Give the location of every parasitized red blood cell.
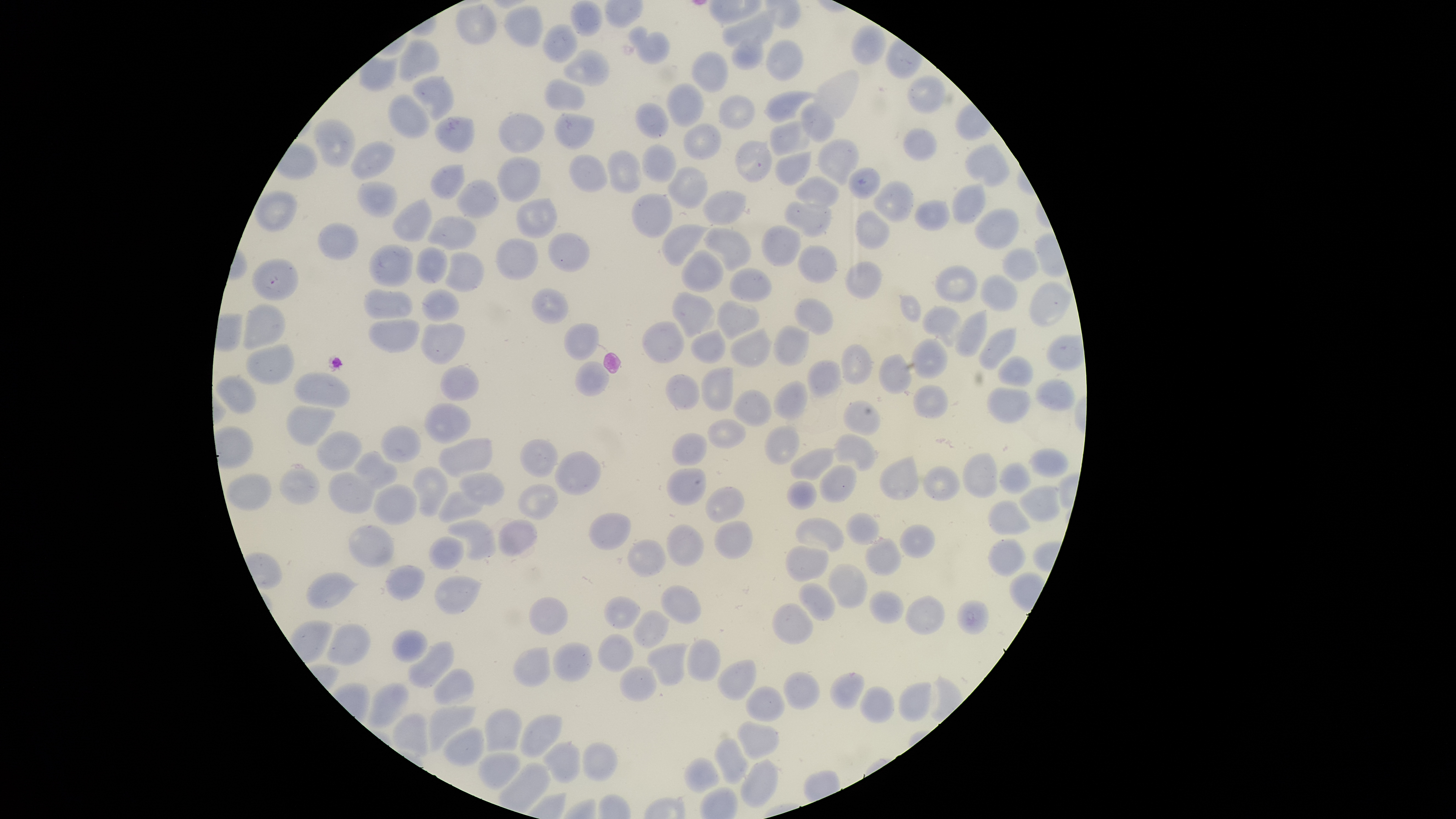
No parasitized red blood cells identified.

Approximate bounding boxes as [left, top, right, bottom] in pixels.
Summary:
  - Uninfected red blood cells: [569, 0, 604, 37], [455, 3, 497, 45], [722, 3, 779, 47], [504, 5, 543, 47], [542, 23, 577, 64], [851, 23, 886, 65], [628, 25, 670, 64], [731, 34, 765, 70], [398, 38, 440, 83], [765, 39, 804, 82], [563, 48, 611, 87], [691, 51, 729, 93], [907, 74, 947, 114], [411, 76, 455, 120], [543, 77, 587, 111], [666, 83, 704, 127], [764, 89, 818, 123], [388, 93, 431, 138], [718, 95, 755, 130], [635, 101, 669, 139], [800, 101, 836, 143], [498, 111, 545, 154], [554, 112, 594, 150], [434, 115, 475, 154], [313, 117, 356, 168], [769, 120, 814, 156], [683, 122, 722, 161], [903, 127, 937, 161], [816, 138, 861, 186], [349, 139, 396, 180], [734, 140, 773, 183], [964, 142, 1010, 187], [641, 144, 677, 182], [606, 150, 644, 194], [774, 151, 813, 187], [568, 154, 609, 193], [496, 155, 541, 203], [429, 164, 465, 200], [667, 167, 708, 209], [848, 167, 881, 200], [794, 175, 841, 210], [456, 178, 499, 218], [356, 180, 397, 218], [872, 180, 914, 223], [951, 183, 986, 225], [702, 188, 747, 225], [252, 190, 299, 232], [630, 192, 673, 239], [392, 196, 433, 243], [516, 197, 557, 239], [914, 199, 950, 232], [783, 201, 832, 238], [974, 207, 1020, 250], [854, 209, 889, 250], [428, 215, 478, 251], [318, 223, 360, 262], [661, 224, 711, 267], [761, 224, 801, 268], [703, 228, 752, 271], [547, 232, 591, 273], [495, 238, 539, 280], [366, 242, 414, 288], [415, 245, 448, 284], [797, 245, 837, 284], [1001, 247, 1040, 283], [680, 249, 725, 292], [445, 251, 485, 293], [251, 258, 299, 301], [844, 261, 883, 300], [934, 264, 978, 303], [729, 267, 773, 303], [979, 274, 1018, 312], [1029, 281, 1073, 327], [421, 287, 459, 322], [531, 287, 569, 324], [363, 288, 414, 320], [671, 291, 715, 338], [794, 298, 834, 336], [716, 299, 759, 340], [242, 303, 286, 352], [921, 305, 962, 348], [954, 309, 988, 357], [368, 318, 421, 353], [642, 320, 684, 364], [421, 322, 465, 364], [564, 323, 600, 360], [772, 325, 811, 366], [978, 326, 1017, 371], [690, 327, 727, 364], [729, 327, 774, 368], [910, 337, 949, 380], [245, 343, 295, 385], [841, 344, 873, 386], [878, 353, 913, 395], [997, 355, 1034, 387], [807, 359, 843, 398], [575, 361, 611, 397], [439, 366, 479, 401], [700, 366, 734, 411], [293, 370, 350, 408], [665, 373, 701, 410], [214, 374, 257, 415], [1035, 378, 1076, 411], [773, 380, 808, 420], [912, 384, 949, 420], [986, 387, 1031, 424], [733, 389, 772, 427], [842, 399, 881, 436], [423, 402, 471, 445], [286, 405, 335, 445], [707, 418, 747, 449], [381, 425, 422, 463], [764, 425, 800, 466], [315, 431, 363, 470], [671, 432, 708, 466], [833, 432, 878, 471], [437, 437, 493, 479], [519, 438, 559, 477], [790, 447, 838, 481], [1027, 448, 1069, 478], [353, 450, 398, 491], [555, 451, 601, 496], [962, 452, 998, 498], [879, 455, 920, 500], [998, 462, 1032, 495], [818, 464, 857, 503], [923, 465, 960, 502], [411, 466, 448, 517], [278, 467, 320, 505], [665, 467, 707, 506], [328, 472, 379, 514], [458, 472, 505, 506], [226, 473, 272, 512], [786, 480, 818, 511], [373, 483, 418, 526], [516, 483, 558, 520], [705, 486, 745, 522], [1018, 486, 1061, 523], [437, 490, 483, 525], [987, 501, 1031, 536], [588, 511, 632, 551], [845, 511, 880, 545], [497, 517, 538, 557], [794, 517, 844, 552], [447, 519, 497, 561], [714, 520, 753, 560], [666, 523, 705, 567], [349, 524, 394, 567], [898, 524, 936, 559], [427, 536, 464, 570], [864, 537, 902, 576], [988, 538, 1026, 577], [627, 539, 667, 578], [785, 544, 829, 582], [827, 563, 868, 609], [386, 564, 425, 602], [306, 572, 359, 609], [433, 575, 482, 616], [798, 582, 836, 621], [660, 585, 702, 624], [869, 589, 905, 624], [905, 594, 945, 634], [602, 596, 641, 630], [528, 597, 568, 636], [956, 598, 990, 634], [771, 603, 814, 645], [632, 610, 671, 649], [325, 621, 372, 667], [392, 630, 428, 663], [597, 634, 633, 672], [686, 638, 720, 683], [406, 640, 454, 689], [551, 642, 593, 682], [645, 643, 688, 686], [512, 646, 550, 687], [717, 659, 757, 701], [619, 664, 657, 702], [433, 668, 475, 706], [784, 671, 821, 711], [829, 672, 866, 710], [367, 681, 410, 728], [898, 681, 932, 721], [746, 685, 786, 722], [859, 685, 895, 724], [428, 706, 476, 752], [484, 708, 522, 753], [519, 713, 563, 758], [735, 720, 781, 761], [442, 727, 485, 768], [714, 738, 750, 784], [542, 741, 581, 783], [581, 741, 618, 781], [478, 752, 521, 790], [684, 757, 720, 794], [740, 759, 779, 809]
  - Preparation: thin blood smear
  - Stain: Giemsa
  - Capture: smartphone photograph through the microscope eyepiece
  - Field of view: single
  - Visible region: circular
  - Image size: 1456×819 pixels